Report the malaria status of this cell.
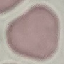

It is uninfected.

Thin blood smear. Photographed with a smartphone camera at the microscope eyepiece. Cell patch, automatically extracted from a larger field of view and resized to 64 × 64 pixels. Giemsa-stained preparation.